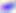

Toxoplasma gondii is seen. Captured at 400x magnification. Micrograph.